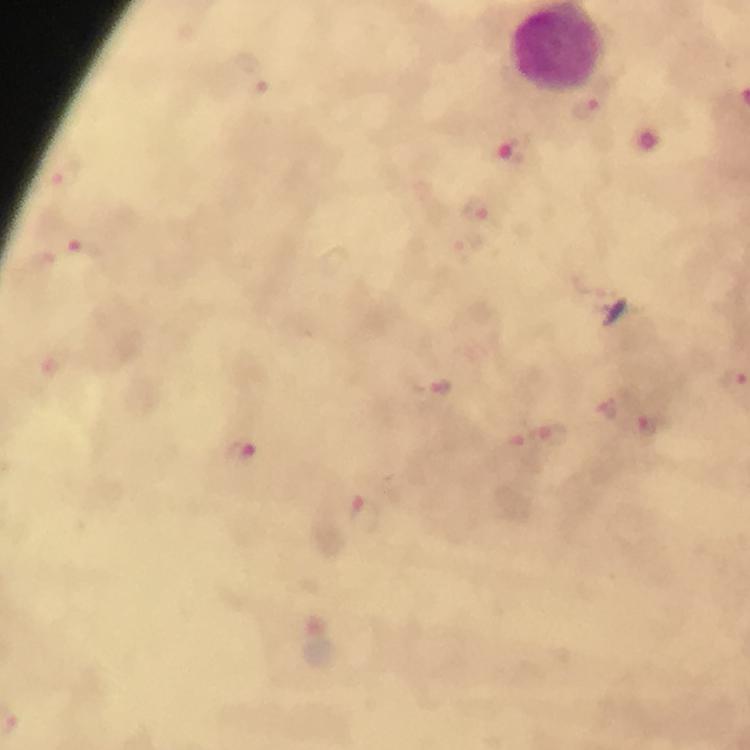

magnification: 100x
cropped_from: a single field of view
image_size: 750×750 pixels
malaria_parasite_locations: 'approximate centers as [x, y] in pixels: [587, 109], [515, 150], [66, 176], [480, 211], [83, 254], [431, 385], [607, 410], [650, 429], [548, 436], [242, 455], [365, 516]'
stain: Giemsa
immersion_oil: used
preparation: thick smear
capture: smartphone mounted on the microscope
context: from a diagnostic examination for malaria